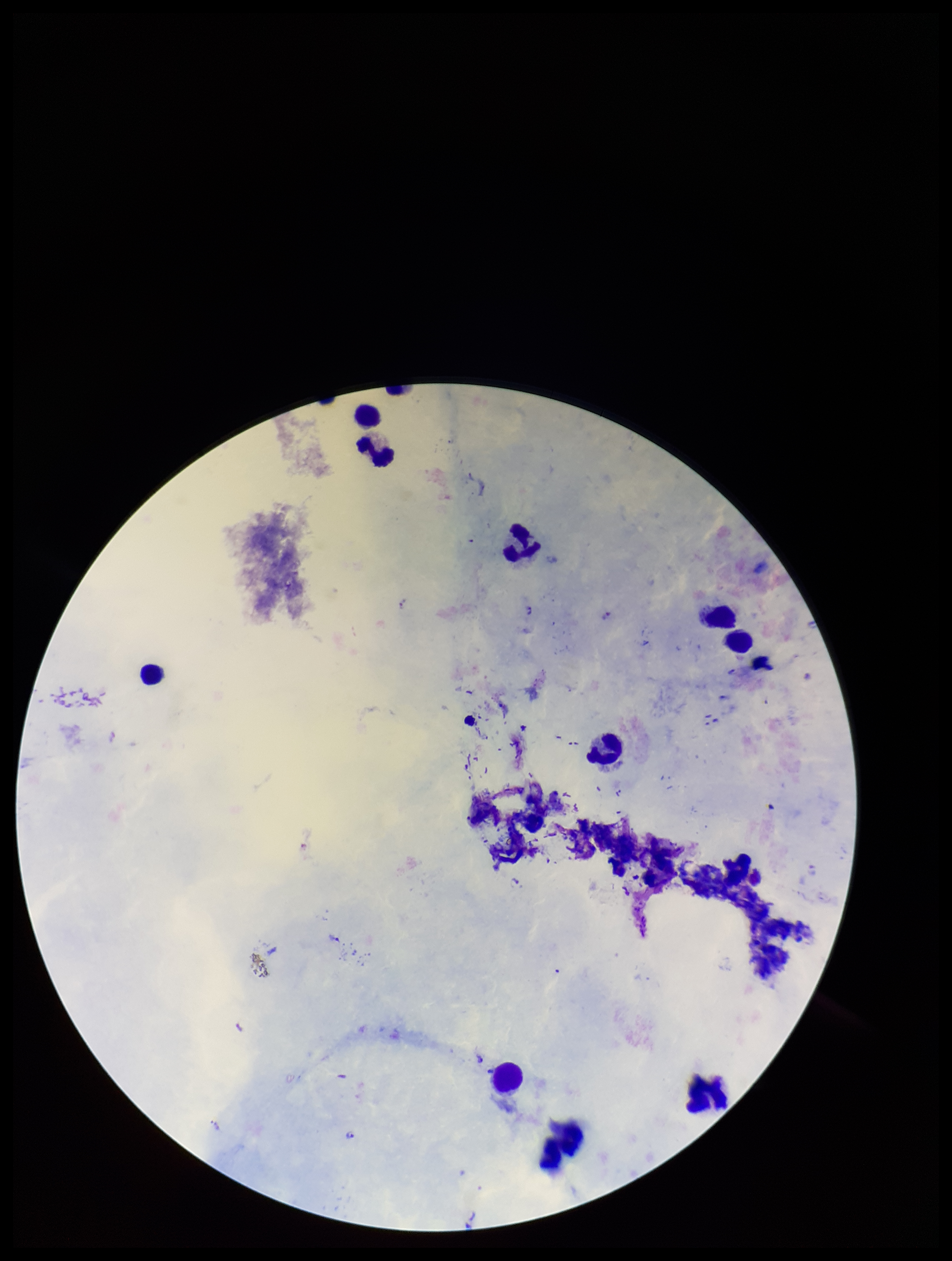
Summary:
  - Patient malaria status: positive
  - Capture: smartphone photograph through the microscope eyepiece
  - Leukocyte count: 12
  - Stain: Giemsa
  - Plasmodium parasites: detected
  - Image size: 952×1261 pixels
  - Field of view: single
  - Parasite count: 4
  - Preparation: thick
  - Species reported for this patient: Plasmodium falciparum